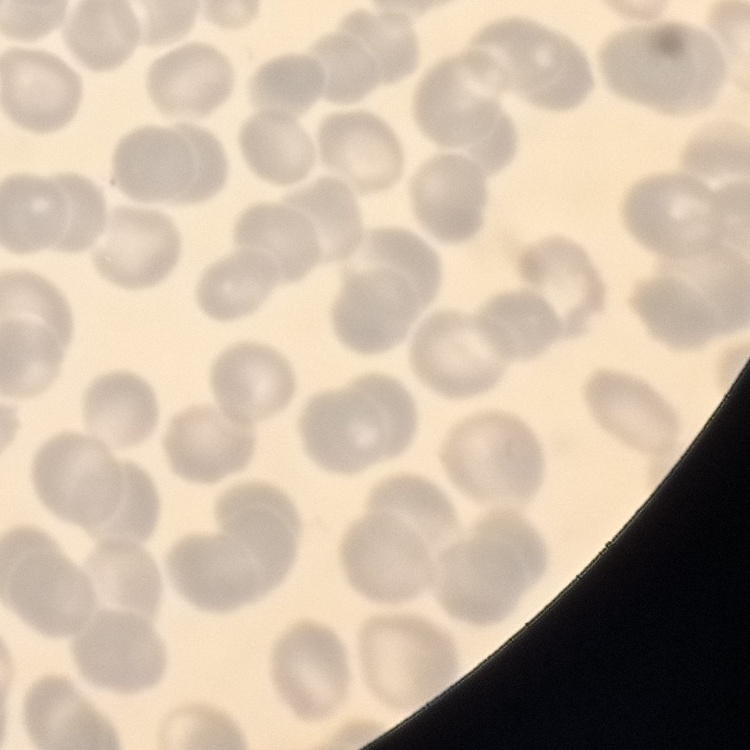
The red blood cells exhibit no rouleaux formation. Thin peripheral smear. Field's or Giemsa stain. One tile cut from a larger photomicrograph.